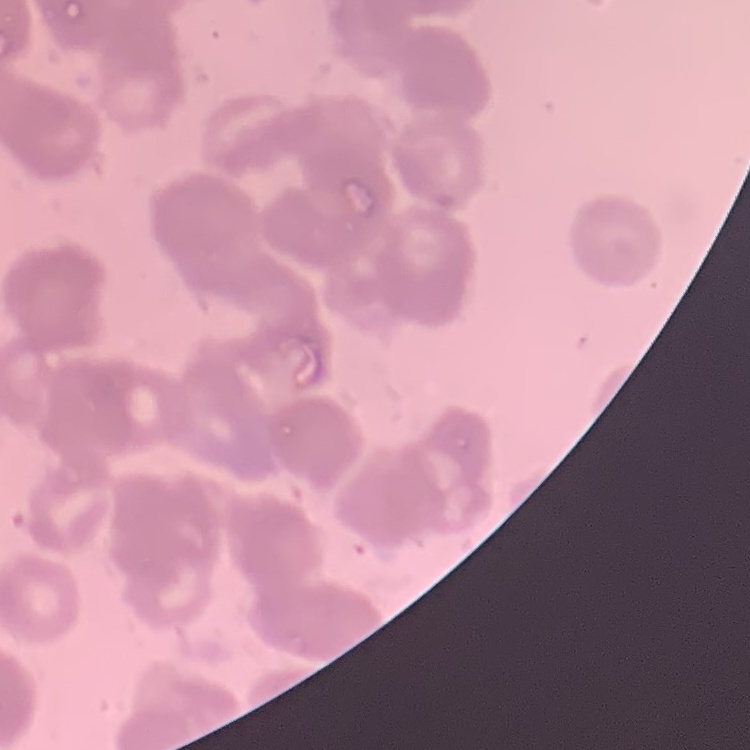

Summary:
  - Erythrocyte morphology: rouleaux formation
  - Stain: Field's or Giemsa
  - Image type: square crop of a larger photomicrograph
  - Preparation: thin blood film